Report the malaria status of this cell.
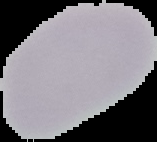
It is uninfected.

image type = segmented cell region on a black background
preparation = thin blood smear
image size = 157×142 pixels